Assess the morphology of the erythrocytes.
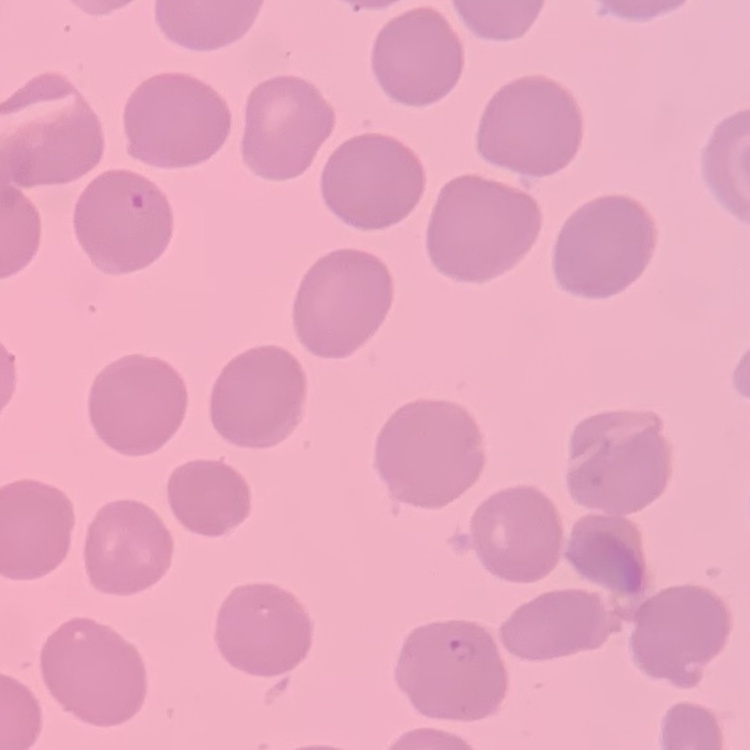

No rouleaux formation.

Summary:
  - Stain: Field's or Giemsa
  - Image type: square crop of a larger photomicrograph
  - Preparation: thin blood smear